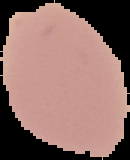

result = no Plasmodium parasites detected
preparation = thin blood film
image type = segmented cell region on a black background
image size = 130×160 pixels